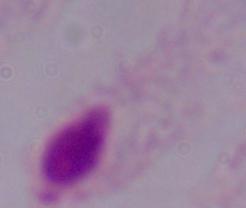 Micrograph. 1000x magnification. A trichomonad is shown.